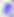
Toxoplasma gondii is shown. Captured at 400x magnification. Micrograph.